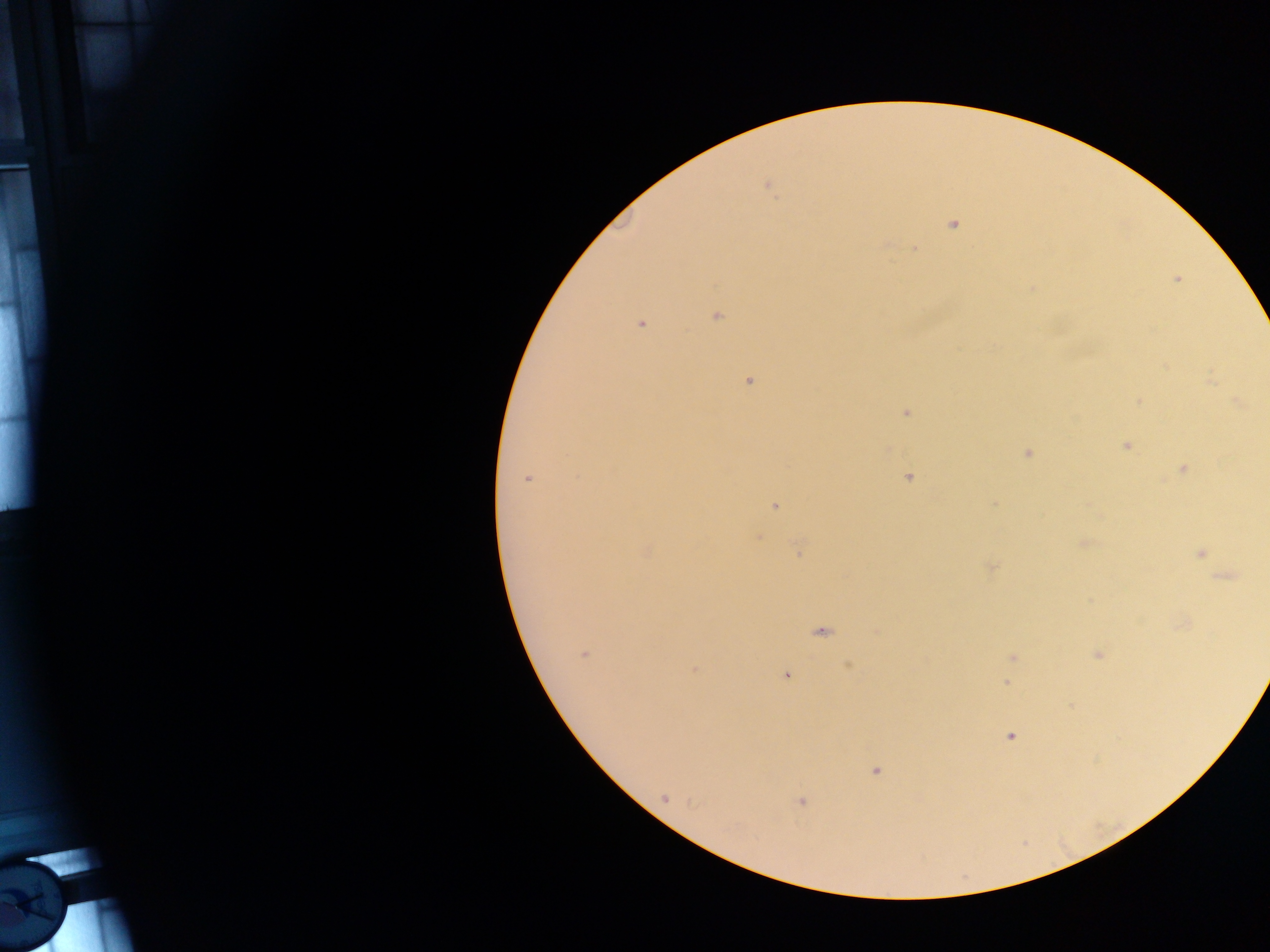
field of view = single
capture = mobile-phone photograph through a microscope
image size = 1270×952 pixels
country = Ghana
preparation = thick blood film
malaria parasite locations = approximate centers as [x, y] in pixels: [768, 187], [953, 224], [916, 247], [1177, 279], [717, 317], [640, 324], [748, 381], [1210, 381], [1140, 401], [1238, 402], [906, 413], [1127, 446], [1027, 453], [1183, 469], [909, 477], [527, 478], [775, 506], [757, 537], [1085, 543], [647, 551], [798, 551], [1201, 553], [990, 567], [1227, 576], [822, 632], [584, 653], [1099, 655], [1012, 657], [850, 666], [694, 669], [787, 675], [1006, 683], [1011, 737], [875, 771], [665, 798], [801, 801]